Assess this cell for malaria.
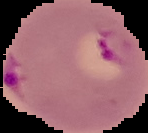
It is parasitized.

Summary:
  - Image type: segmented cell region on a black background
  - Image size: 148×133 pixels
  - Preparation: thin blood smear